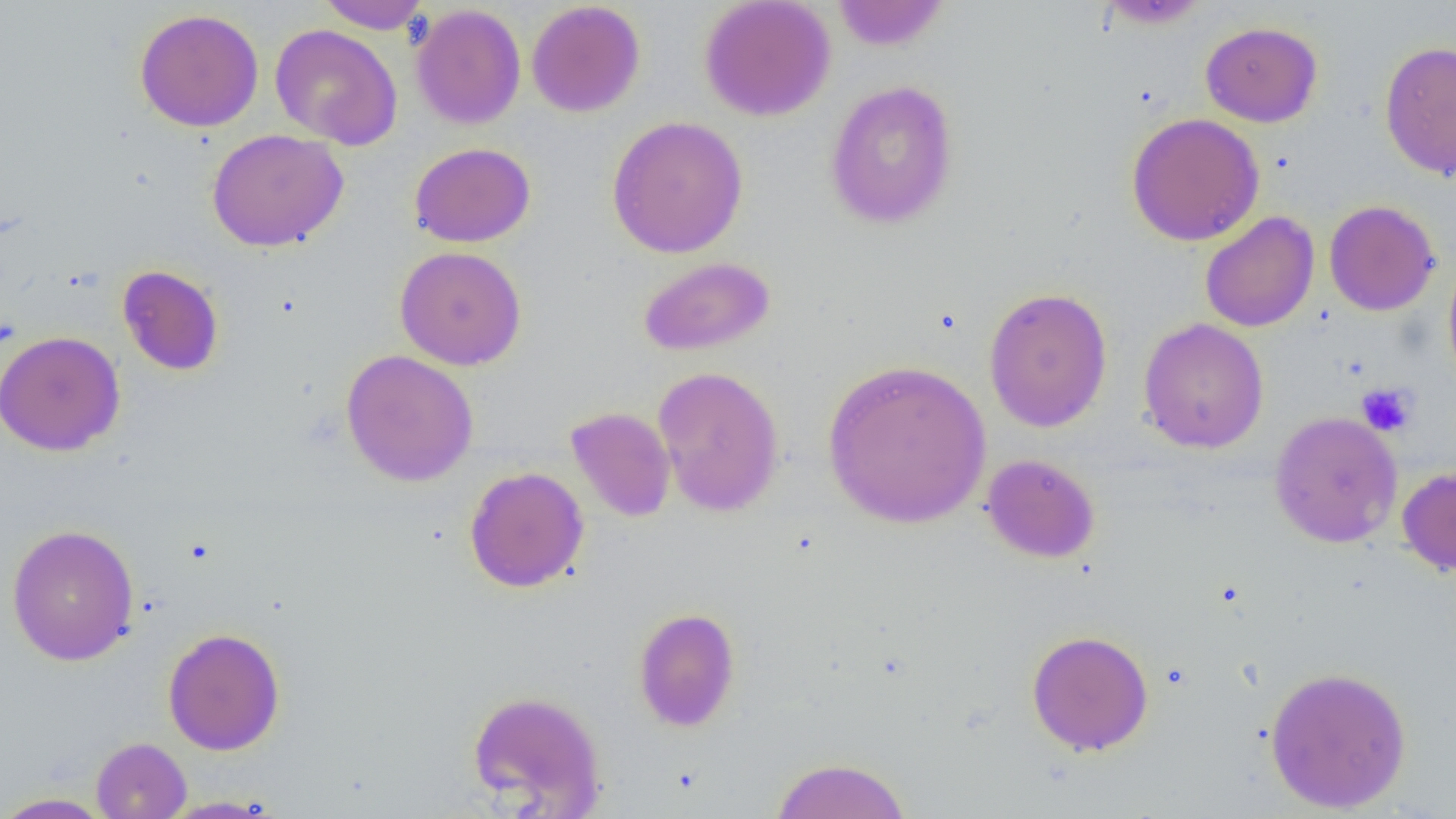

Approximate bounding boxes as [x1, y1, x2, y2] in pixels. Platelet locations: [1356, 382, 1416, 436]. Uninfected red blood cell locations: [315, 0, 432, 33], [699, 0, 836, 122], [831, 0, 950, 52], [526, 1, 646, 117], [1097, 1, 1212, 29], [410, 4, 526, 130], [134, 8, 264, 132], [1200, 21, 1323, 127], [270, 23, 403, 149], [1379, 41, 1456, 180], [824, 79, 960, 230], [1125, 112, 1265, 246], [606, 115, 748, 258], [206, 128, 349, 252], [409, 142, 535, 247], [1324, 200, 1440, 316], [1199, 212, 1320, 332], [394, 246, 527, 370], [1442, 253, 1456, 393], [638, 256, 775, 356], [117, 264, 225, 377], [983, 287, 1113, 432], [1138, 318, 1269, 454], [0, 330, 125, 456], [340, 349, 479, 487], [822, 358, 992, 529], [652, 365, 785, 517], [565, 406, 676, 522], [1269, 411, 1402, 548], [981, 453, 1101, 564], [1397, 465, 1456, 578], [464, 466, 589, 593], [6, 523, 140, 666], [633, 607, 741, 732], [162, 627, 286, 756], [1026, 629, 1154, 756], [1264, 665, 1413, 813], [467, 689, 606, 815], [91, 737, 191, 819], [770, 756, 912, 818], [0, 792, 115, 818], [157, 795, 285, 817]. Slide-level diagnosis: no evidence of blood parasites. Thin blood film. Captured at 1000x magnification. One field of a larger specimen. Optical microscopy. Image is 1456×819 pixels.